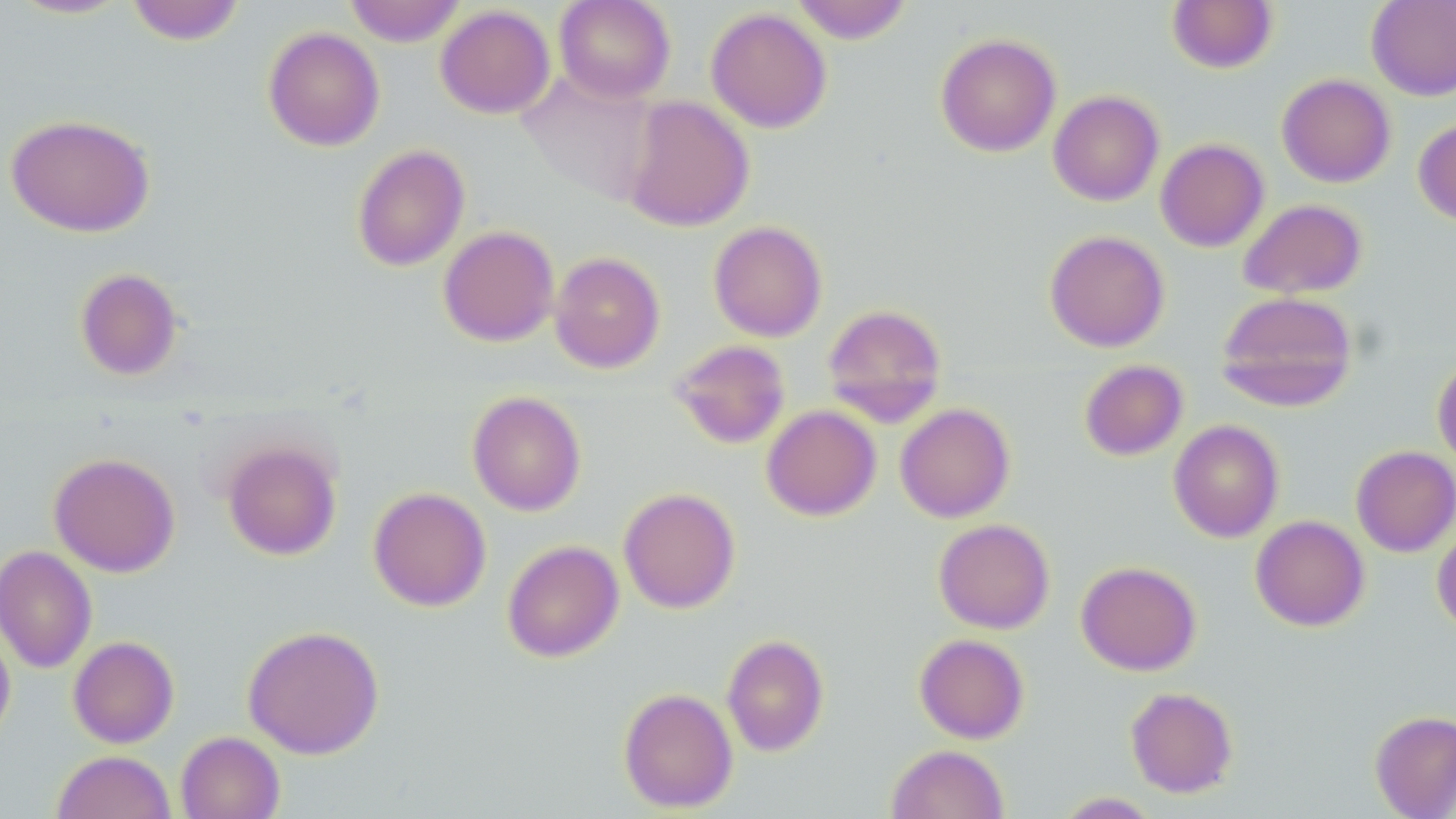
slide-level diagnosis = no evidence of blood parasites
preparation = thin blood smear
field of view = one of a larger specimen
modality = optical microscopy
image size = 1456×819 pixels
magnification = 1000x
uninfected red blood cell locations = approximate bounding boxes as (x1,y1)-(x2,y2) corner pairs in pixels: (7,0)-(134,20), (125,0)-(246,45), (344,0)-(466,46), (554,0)-(675,104), (791,0)-(913,43), (1167,0)-(1277,74), (1366,0)-(1456,101), (435,4)-(556,119), (706,7)-(832,133), (263,26)-(385,151), (935,32)-(1061,157), (516,69)-(660,207), (1277,73)-(1396,188), (1048,90)-(1164,206), (621,95)-(754,232), (5,113)-(156,237), (1413,117)-(1456,226), (1155,138)-(1269,252), (352,143)-(470,272), (1238,198)-(1367,299), (708,220)-(827,342), (438,225)-(559,347), (1044,229)-(1170,352), (549,251)-(666,373), (75,267)-(183,381), (1216,291)-(1358,411), (822,303)-(947,425), (670,339)-(791,449), (1432,357)-(1456,468), (1078,359)-(1188,461), (467,390)-(586,516), (894,403)-(1015,523), (761,404)-(881,521), (1168,419)-(1285,542), (222,440)-(342,560), (1351,446)-(1456,557), (48,451)-(180,577), (368,486)-(491,611), (618,486)-(741,613), (1250,515)-(1370,631), (933,519)-(1055,634), (1432,524)-(1456,635), (501,539)-(624,663), (0,545)-(97,673), (1075,561)-(1201,675), (0,621)-(16,750), (242,624)-(385,759), (721,633)-(829,756), (914,633)-(1029,744), (68,635)-(179,748), (618,686)-(738,813), (1125,686)-(1238,798), (1370,710)-(1456,818), (175,730)-(285,819), (886,744)-(1010,819), (51,750)-(176,819), (1053,792)-(1163,818)
stain = May-Grünwald-Giemsa